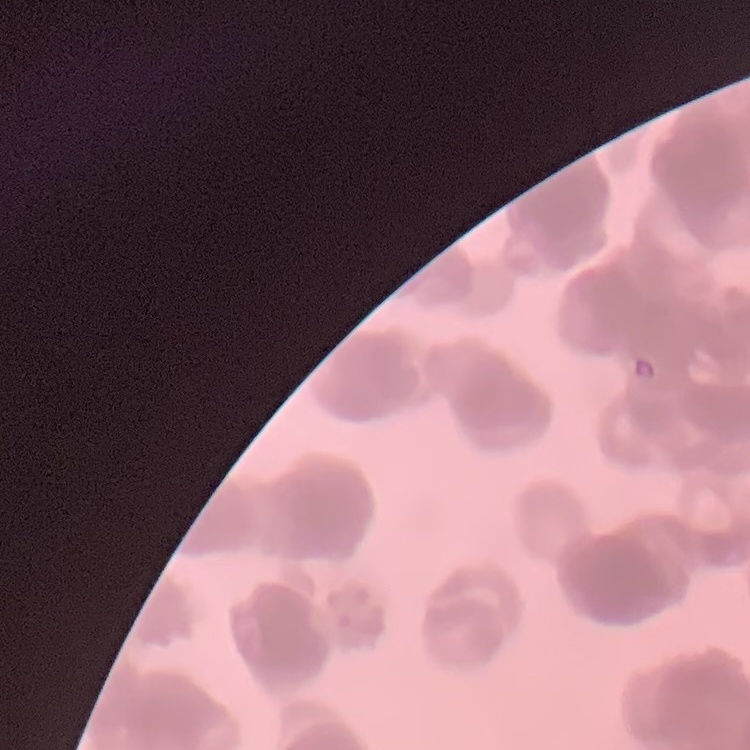

The erythrocytes show rouleaux formation. Thin blood film. Field's or Giemsa stain. One tile cut from a larger photomicrograph.